Give the extent of all uninfected red blood cells.
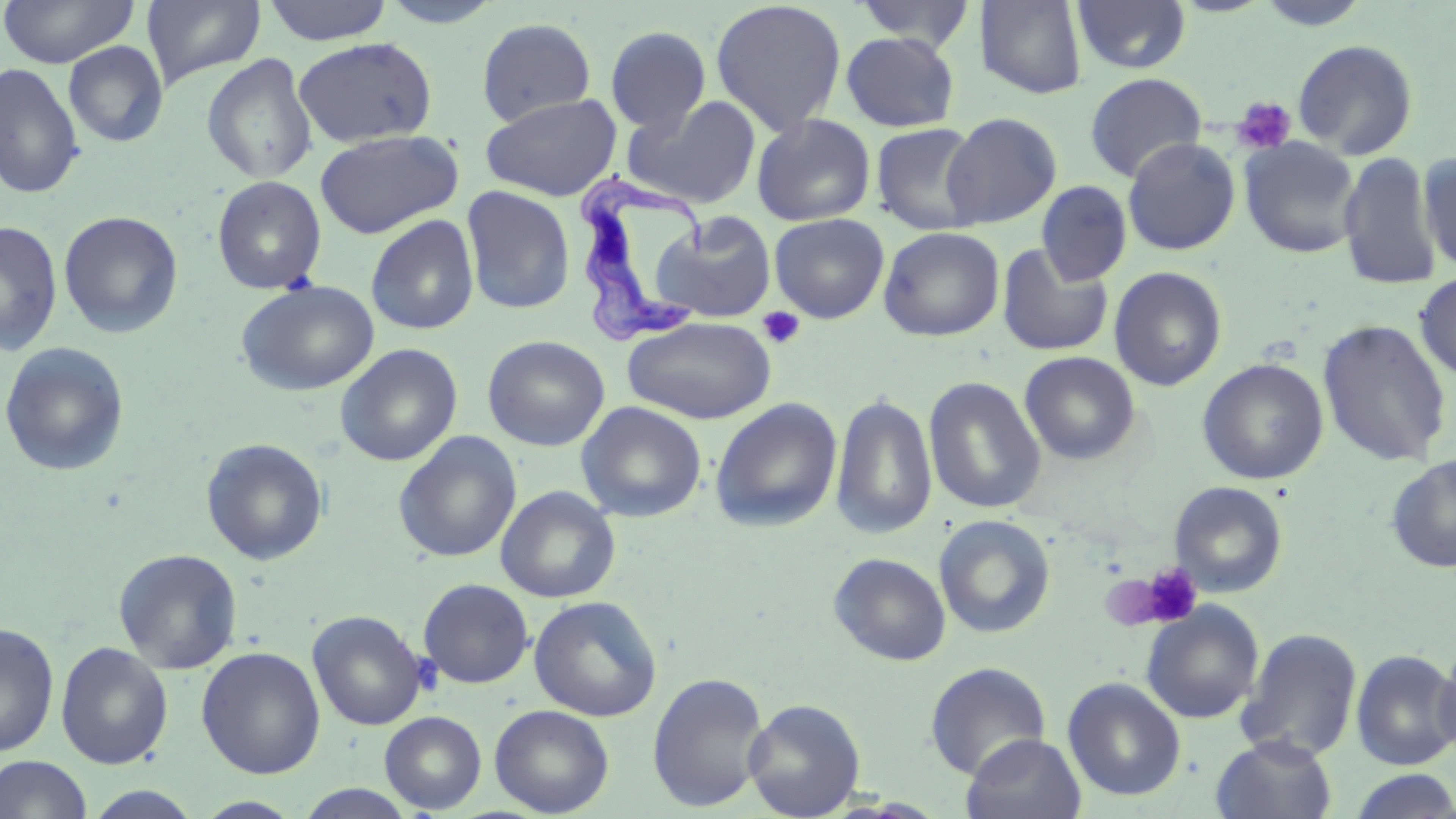

Approximate bounding boxes as (x1, y1, x2, y2) in pixels.
Uninfected red blood cells: (0, 0, 139, 67), (142, 0, 267, 89), (263, 0, 393, 45), (377, 0, 506, 28), (710, 0, 848, 137), (853, 0, 977, 51), (1072, 0, 1192, 75), (1254, 0, 1371, 31), (975, 1, 1088, 99), (477, 17, 596, 126), (604, 25, 712, 134), (841, 31, 960, 132), (293, 36, 438, 148), (1292, 39, 1418, 159), (63, 41, 168, 147), (202, 54, 317, 184), (0, 63, 84, 200), (1084, 72, 1207, 183), (480, 93, 622, 201), (622, 96, 762, 209), (942, 112, 1062, 229), (751, 114, 876, 226), (871, 123, 985, 235), (315, 129, 463, 238), (1122, 137, 1241, 255), (1239, 138, 1362, 258), (1417, 151, 1455, 276), (1338, 152, 1442, 292), (212, 175, 327, 294), (1036, 182, 1131, 286), (461, 185, 576, 315), (59, 210, 183, 339), (649, 210, 774, 322), (769, 213, 889, 323), (366, 215, 480, 335), (0, 221, 63, 356), (879, 226, 1005, 341), (996, 243, 1113, 356), (1109, 267, 1227, 391), (1414, 270, 1456, 382), (235, 279, 379, 396), (622, 315, 777, 424), (1317, 317, 1453, 469), (483, 335, 610, 451), (0, 342, 130, 477), (335, 343, 462, 467), (1020, 351, 1140, 465), (1198, 358, 1328, 484), (923, 376, 1047, 515), (830, 392, 937, 540), (710, 397, 843, 533), (576, 401, 707, 523), (392, 431, 522, 563), (201, 438, 329, 566), (1386, 455, 1456, 573), (1170, 481, 1288, 597), (495, 485, 621, 602), (933, 514, 1055, 639), (113, 548, 243, 673), (828, 552, 952, 666), (418, 578, 534, 688), (528, 595, 662, 721), (1141, 602, 1264, 724), (308, 610, 427, 731), (0, 622, 60, 757), (1236, 628, 1362, 763), (1434, 638, 1456, 762), (55, 642, 173, 769), (196, 646, 325, 779), (1351, 649, 1456, 770), (924, 662, 1051, 780), (647, 672, 769, 812), (1062, 677, 1186, 801), (743, 698, 865, 818), (489, 704, 614, 817), (379, 711, 487, 813), (961, 733, 1087, 819), (1211, 735, 1338, 819), (0, 755, 93, 819), (1345, 770, 1456, 818), (293, 783, 422, 818), (83, 786, 204, 818), (192, 796, 305, 818).

Platelet locations: (1231, 96, 1298, 155), (757, 306, 805, 349), (1138, 563, 1203, 628), (1099, 571, 1176, 630). Trypanosoma brucei locations: (579, 167, 709, 346). Slide-level diagnosis: Trypanosoma brucei. Light microscopy. May-Grünwald-Giemsa-stained preparation. Thin blood film. Captured at 1000x magnification. One field of a larger specimen. Image is 1456×819 pixels.